Classify this cell by malaria status.
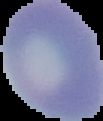
Uninfected.

From a thin blood film. The area outside the segmented cell region is set to black. Image is 103×121 pixels.